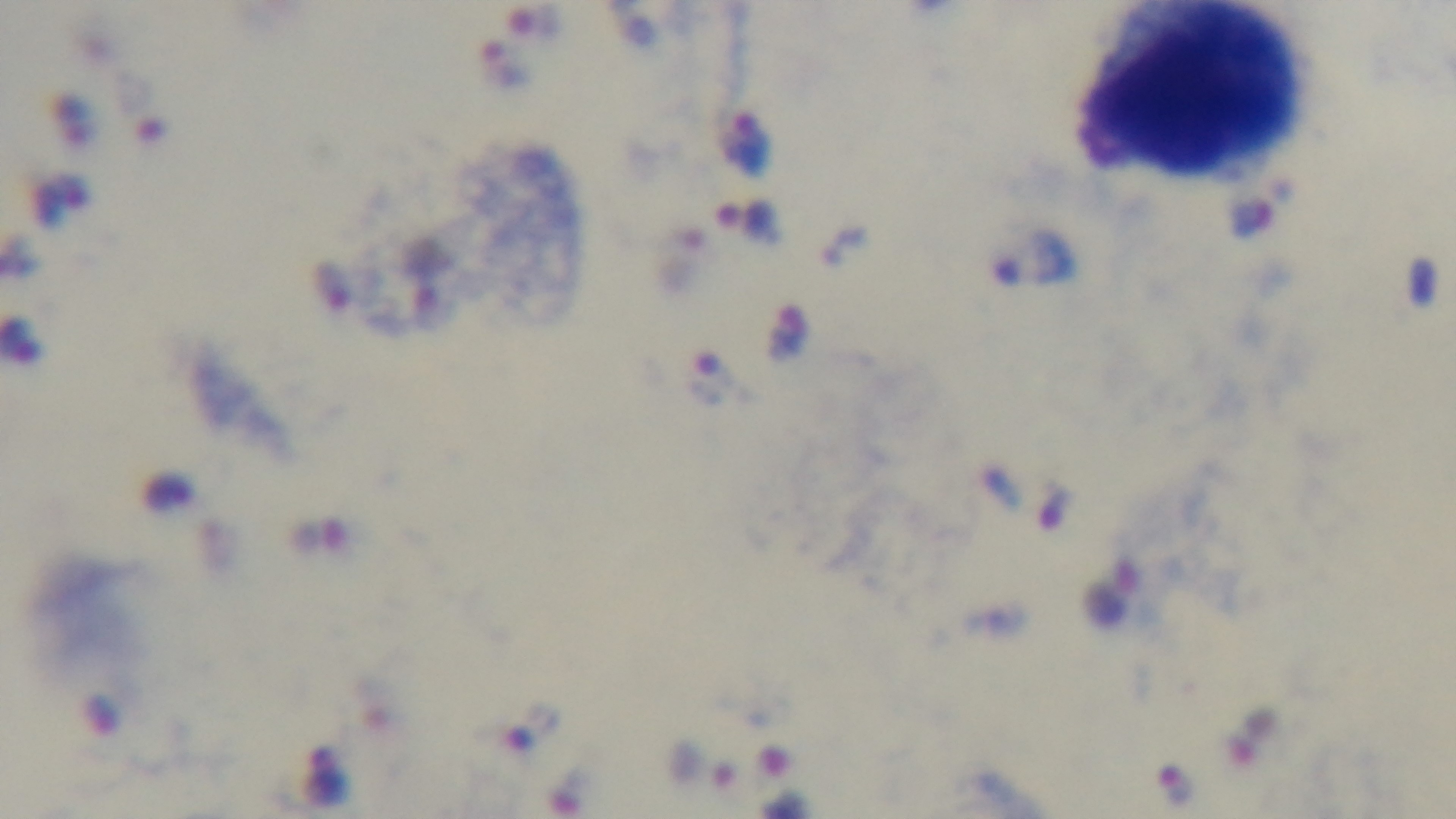
Malaria status: infected. Light microscopy. Oil-immersion objective, 100x. Giemsa stain. Captured with a mounted 4K digital camera. Single field of view. Preparation: thick blood film.